Identify the parasite.
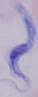

This is a trypanosome.

Photomicrograph. Captured at 1000x magnification.